Report the malaria status of this cell.
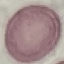
It is uninfected.

Summary:
  - Image type: cell patch, automatically extracted from a larger field of view and resized to 64 × 64 pixels
  - Preparation: thin blood film
  - Capture: smartphone camera at the microscope eyepiece
  - Stain: Giemsa